Report the malaria status of this cell.
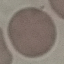
It is uninfected.

image type = cell patch, automatically extracted from a larger field of view and resized to 64 × 64 pixels
stain = Giemsa
preparation = thin blood film
capture = smartphone through the microscope eyepiece